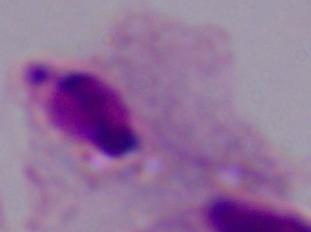

A trichomonad is shown. 1000x magnification. Micrograph.